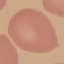
Malaria status: uninfected. Cell patch, automatically extracted from a larger field of view and resized to 64 × 64 pixels. Thin smear of blood. Giemsa-stained preparation. Photographed with a smartphone camera at the microscope eyepiece.